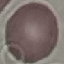

malaria status = uninfected
capture = smartphone camera at the microscope eyepiece
image type = cell patch, automatically extracted from a larger field of view and resized to 64 × 64 pixels
stain = Giemsa
preparation = thin smear